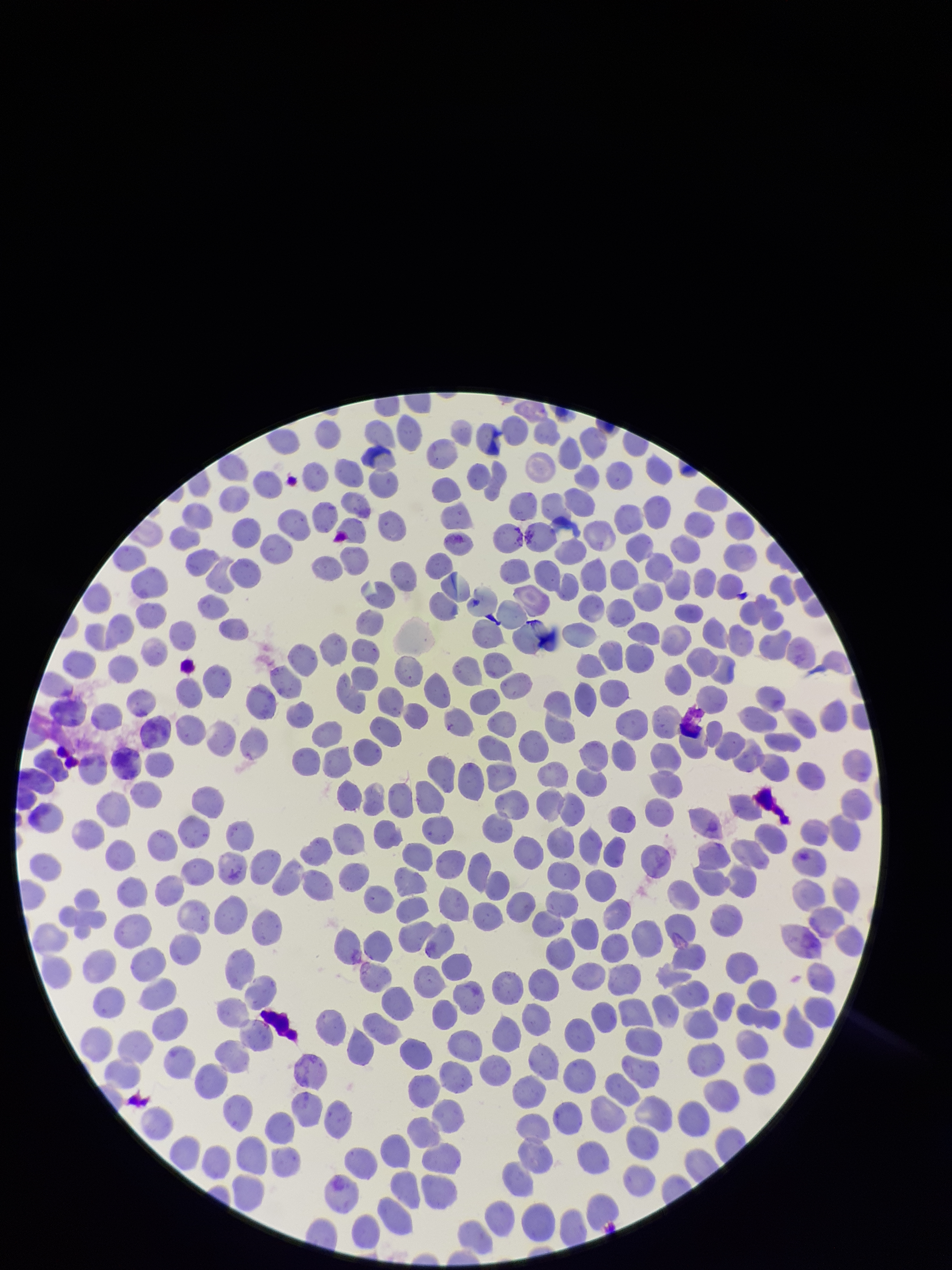
Summary:
  - Capture: smartphone photograph through the microscope eyepiece
  - Patient malaria status: negative
  - Stain: Giemsa
  - Field of view: single
  - Parasitized red blood cells: none seen
  - Parasitized red blood cell count: 0
  - Image size: 952×1270 pixels
  - Red blood cell count: 243
  - Preparation: thin blood smear